Locate every malaria parasite.
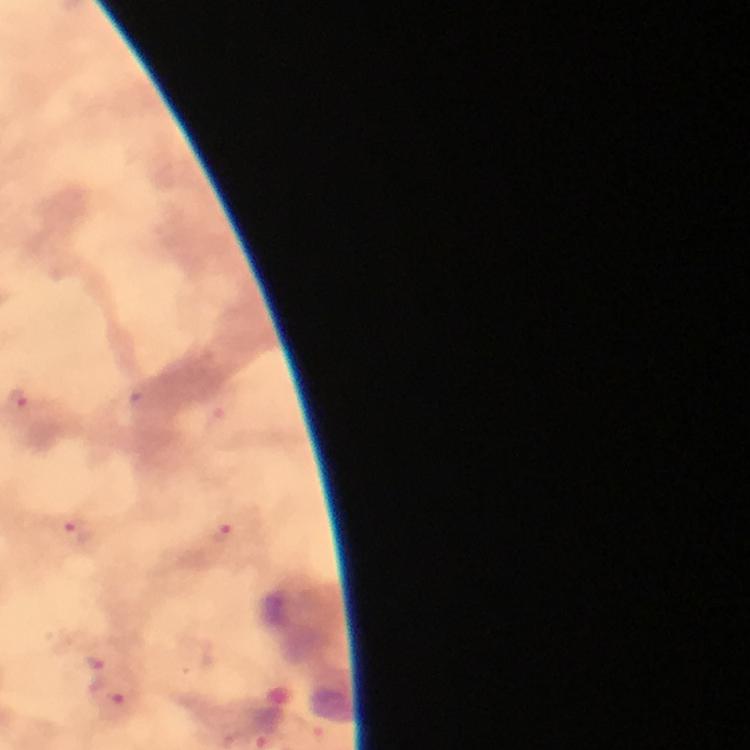
Approximate centers as (x, y) in pixels.
Malaria parasites: (223, 533), (73, 534), (94, 671), (121, 703).

preparation = thick blood smear
capture = smartphone camera through the microscope
immersion oil = applied
stain = Giemsa
image size = 750×750 pixels
context = from a diagnostic examination for malaria
cropped from = one field of view
magnification = 100x